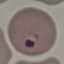

Malaria status: parasitized. Giemsa-stained preparation. Thin smear of blood. Photographed with a smartphone camera at the microscope eyepiece. Cell patch, automatically extracted from a larger field of view and resized to 64 × 64 pixels.